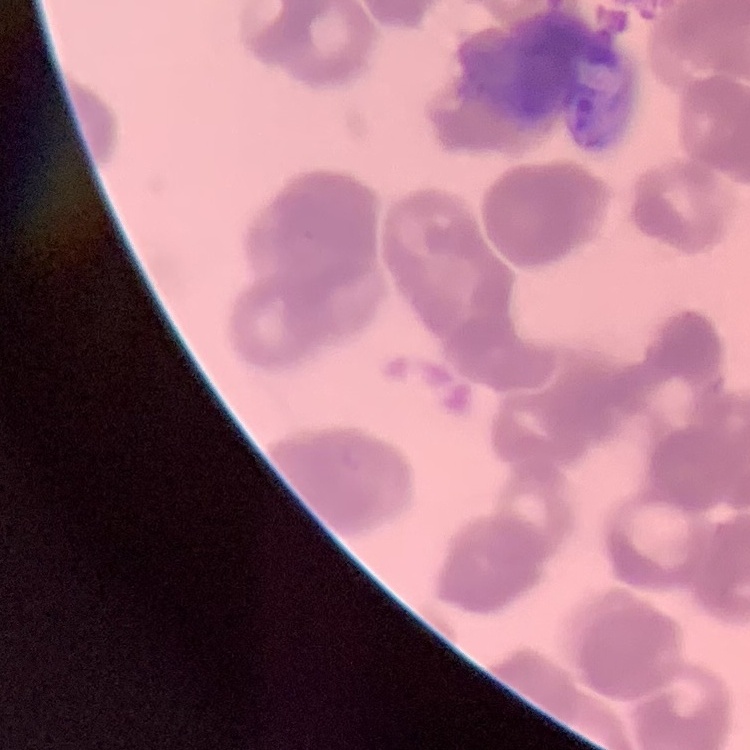
The erythrocytes show rouleaux formation. Stained with either Field's or Giemsa. Thin blood film. One tile cut from a larger photomicrograph.